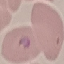
Summary:
  - Malaria status: parasitized
  - Stain: Giemsa
  - Image type: cell patch, automatically extracted from a larger field of view and resized to 64 × 64 pixels
  - Capture: smartphone camera at the microscope eyepiece
  - Preparation: thin blood smear